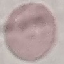

result: no malaria parasites seen
image_type: cell patch, automatically extracted from a larger field of view and resized to 64 × 64 pixels
capture: smartphone through the microscope eyepiece
stain: Giemsa
preparation: thin blood film